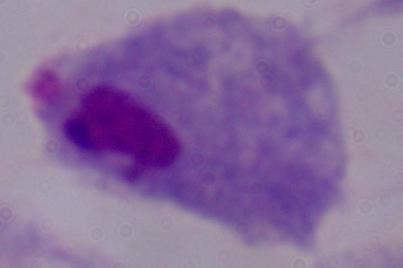

{
  "modality": "photomicrograph",
  "magnification": "1000x",
  "identification": "trichomonad"
}